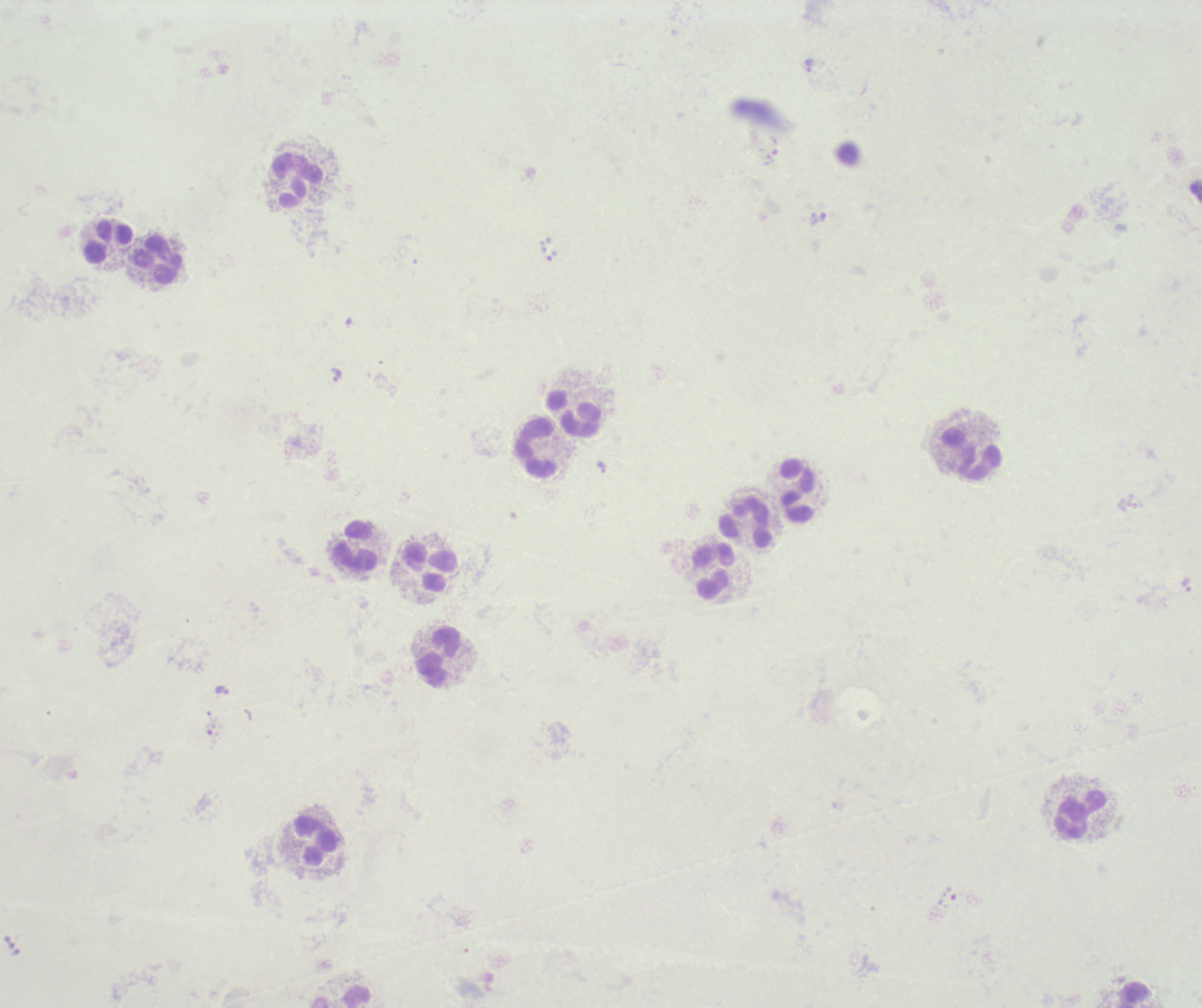

Approximate object centers, in pixels from the top-left corner.
Summary:
  - Trophozoite locations: (x=809, y=64), (x=336, y=374), (x=222, y=691)
  - Leukocyte locations: (x=295, y=181), (x=107, y=240), (x=157, y=260), (x=573, y=414), (x=536, y=448), (x=971, y=456), (x=796, y=491), (x=747, y=524), (x=355, y=547), (x=429, y=569), (x=713, y=571), (x=439, y=658), (x=1080, y=815), (x=313, y=841)
  - Image size: 1202×1008 pixels
  - Preparation: thick smear of blood
  - Context: previously used in an actual diagnosis
  - Field of view: single
  - Background quality: poor
  - Result: Plasmodium parasites identified
  - Magnification: 100x
  - Stain: Romanowsky